Classify this cell by malaria status.
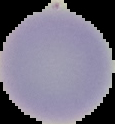

Uninfected.

image_type: cell region segmented out of the field of view; surrounding area masked to black
image_size: 115×124 pixels
preparation: thin blood smear